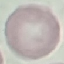

{
  "malaria_status": "uninfected",
  "image_type": "automatically extracted cell patch, resized to 64 × 64 pixels",
  "stain": "Giemsa",
  "capture": "smartphone through the microscope eyepiece",
  "preparation": "thin blood smear"
}